Locate and identify every blood parasite.
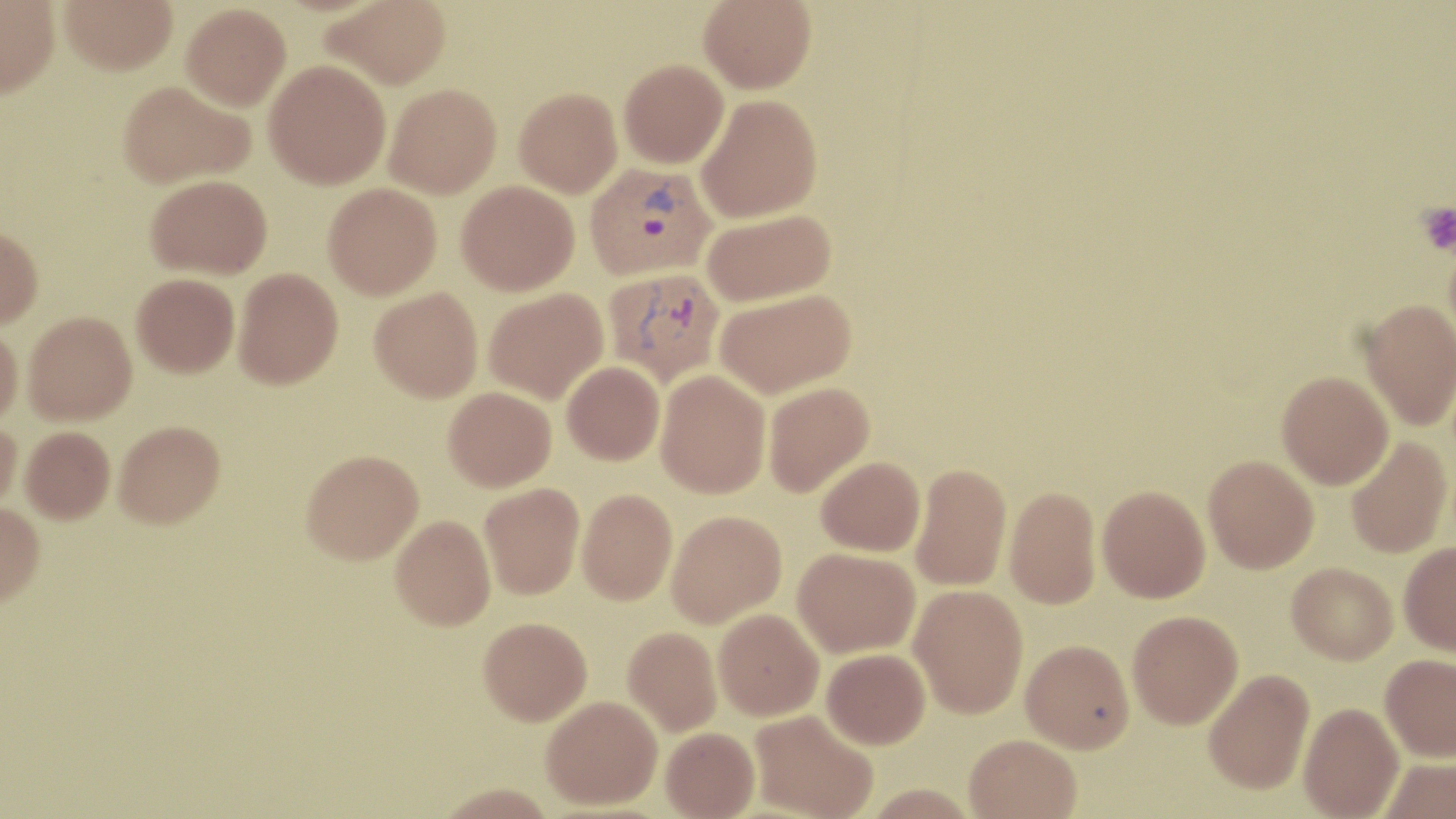

Approximate bounding boxes as named x1/y1/x2/y2 corners in pixels.
Plasmodium vivax-infected red blood cells: (x1=585, y1=162, x2=716, y2=280), (x1=603, y1=267, x2=726, y2=388).
No Plasmodium falciparum, Plasmodium ovale, Plasmodium malariae, Babesia divergens, or Trypanosoma brucei observed.

{
  "slide_level_diagnosis": "Plasmodium vivax",
  "stain": "May-Grünwald-Giemsa",
  "magnification": "1000x",
  "preparation": "thin blood film",
  "field_of_view": "single",
  "platelet_locations": "approximate bounding boxes as named x1/y1/x2/y2 corners in pixels: (x1=1416, y1=202, x2=1456, y2=255)",
  "uninfected_red_blood_cell_locations": "approximate bounding boxes as named x1/y1/x2/y2 corners in pixels: (x1=59, y1=0, x2=177, y2=75), (x1=321, y1=0, x2=451, y2=89), (x1=699, y1=0, x2=816, y2=93), (x1=0, y1=1, x2=59, y2=97), (x1=181, y1=3, x2=291, y2=111), (x1=619, y1=58, x2=728, y2=168), (x1=263, y1=60, x2=390, y2=189), (x1=118, y1=80, x2=254, y2=188), (x1=384, y1=84, x2=501, y2=198), (x1=514, y1=87, x2=622, y2=197), (x1=696, y1=94, x2=823, y2=223), (x1=146, y1=175, x2=272, y2=279), (x1=456, y1=181, x2=579, y2=295), (x1=323, y1=183, x2=441, y2=299), (x1=702, y1=208, x2=836, y2=306), (x1=0, y1=226, x2=43, y2=329), (x1=234, y1=267, x2=344, y2=389), (x1=132, y1=273, x2=239, y2=377), (x1=370, y1=287, x2=483, y2=402), (x1=483, y1=288, x2=608, y2=404), (x1=715, y1=288, x2=856, y2=398), (x1=1359, y1=299, x2=1456, y2=430), (x1=23, y1=312, x2=137, y2=424), (x1=0, y1=326, x2=23, y2=427), (x1=562, y1=362, x2=664, y2=465), (x1=655, y1=369, x2=770, y2=498), (x1=1277, y1=371, x2=1394, y2=489), (x1=763, y1=382, x2=874, y2=497), (x1=444, y1=387, x2=556, y2=492), (x1=0, y1=418, x2=23, y2=516), (x1=114, y1=420, x2=225, y2=528), (x1=20, y1=426, x2=115, y2=523), (x1=1345, y1=435, x2=1451, y2=558), (x1=301, y1=449, x2=424, y2=564), (x1=1203, y1=454, x2=1319, y2=573), (x1=816, y1=456, x2=925, y2=556), (x1=910, y1=462, x2=1011, y2=591), (x1=480, y1=483, x2=584, y2=599), (x1=1004, y1=485, x2=1101, y2=610), (x1=1097, y1=486, x2=1210, y2=602), (x1=577, y1=489, x2=677, y2=605), (x1=0, y1=502, x2=44, y2=607), (x1=666, y1=510, x2=787, y2=628), (x1=390, y1=515, x2=495, y2=630), (x1=1398, y1=541, x2=1456, y2=655), (x1=793, y1=547, x2=920, y2=657), (x1=1286, y1=562, x2=1397, y2=664), (x1=909, y1=584, x2=1028, y2=718), (x1=714, y1=608, x2=823, y2=720), (x1=1128, y1=610, x2=1243, y2=728), (x1=479, y1=616, x2=592, y2=725), (x1=623, y1=626, x2=722, y2=736), (x1=1021, y1=639, x2=1135, y2=752), (x1=822, y1=648, x2=930, y2=749), (x1=1380, y1=653, x2=1456, y2=761), (x1=1203, y1=667, x2=1314, y2=794), (x1=541, y1=695, x2=662, y2=809), (x1=1298, y1=702, x2=1404, y2=819), (x1=750, y1=709, x2=877, y2=819), (x1=661, y1=727, x2=759, y2=819), (x1=963, y1=734, x2=1081, y2=819), (x1=1377, y1=758, x2=1456, y2=819)",
  "image_size": "1456×819 pixels",
  "modality": "optical microscopy"
}